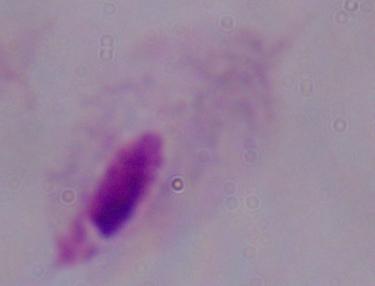

Summary:
  - Identification: trichomonad
  - Magnification: 1000x
  - Modality: photomicrograph